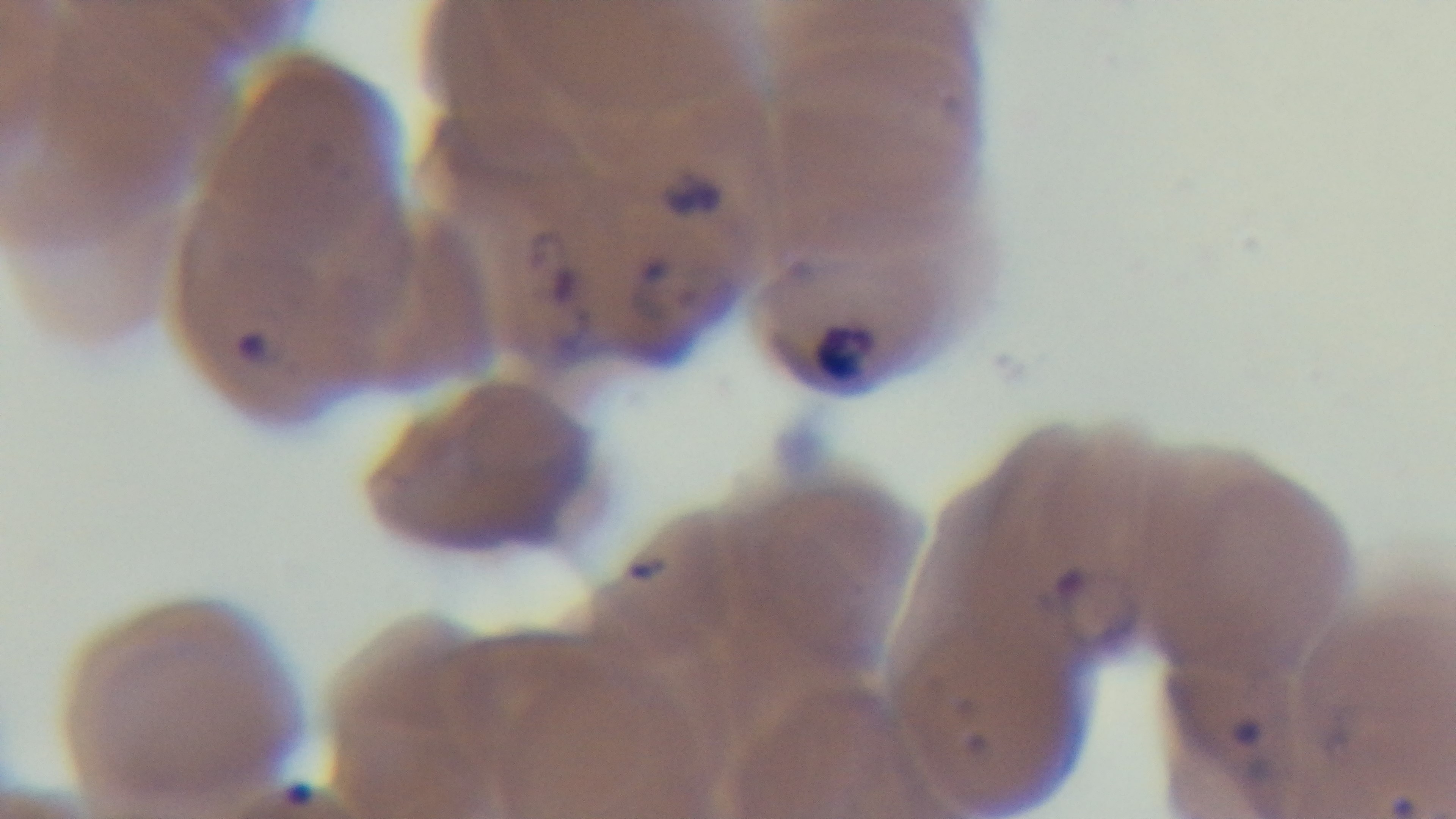

Summary:
  - Preparation: thin blood film
  - Stain: Giemsa
  - Objective: 100x oil immersion
  - Malaria status: positive
  - Field of view: one from the slide
  - Modality: light microscopy
  - Capture: mounted 4K digital camera